Identify the cell.
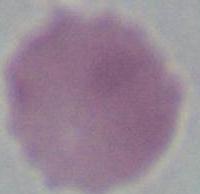
This is an erythrocyte.

modality = photomicrograph
magnification = 1000x